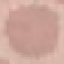

malaria status = uninfected
stain = Giemsa
capture = smartphone through the microscope eyepiece
preparation = thin smear
image type = automatically extracted cell patch, resized to 64 × 64 pixels